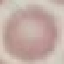
Malaria status: uninfected. Thin blood film. Cell patch, automatically extracted from a larger field of view and resized to 64 × 64 pixels. Acquired by smartphone through the microscope eyepiece. Giemsa stain.